Report the malaria status of this cell.
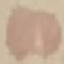

It is uninfected.

{
  "capture": "smartphone through the microscope eyepiece",
  "image_type": "cell patch, automatically extracted from a larger field of view and resized to 64 × 64 pixels",
  "stain": "Giemsa",
  "preparation": "thin blood film"
}